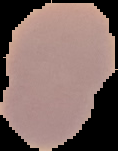 Image is 118×151 pixels. Malaria status: uninfected. From a thin blood smear. Cell region segmented out of the field of view; the surrounding area is masked to black.